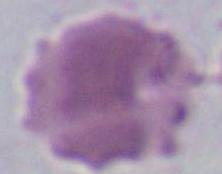

Summary:
  - Identification: red blood cell
  - Modality: photomicrograph
  - Magnification: 1000x